Name the parasite shown.
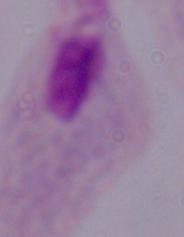

A trichomonad.

1000x magnification. Photomicrograph.